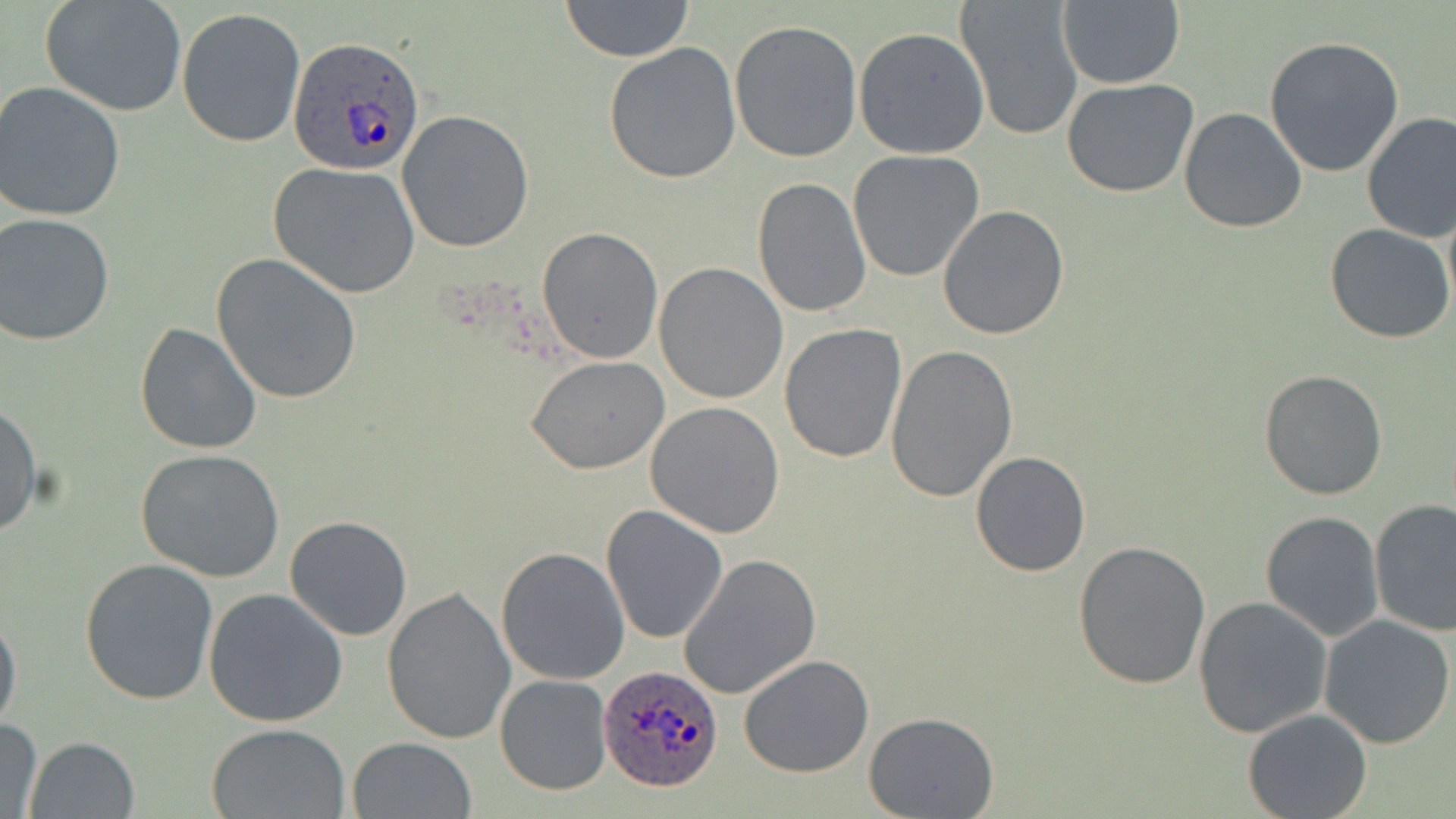

slide-level diagnosis = Plasmodium ovale
field of view = one of a larger specimen
uninfected red blood cell locations = approximate bounding boxes as (x1,y1)-(x2,y2) corner pairs in pixels: (40,0)-(189,118), (559,0)-(695,64), (954,0)-(1085,142), (1055,0)-(1185,89), (176,8)-(308,148), (728,19)-(862,163), (853,27)-(989,159), (1264,35)-(1405,178), (604,41)-(743,184), (1062,77)-(1199,198), (0,82)-(126,223), (1179,108)-(1307,231), (397,110)-(534,252), (1360,111)-(1456,243), (848,149)-(985,282), (268,162)-(420,298), (752,177)-(871,319), (938,204)-(1070,340), (1,214)-(115,346), (1325,224)-(1455,345), (536,226)-(665,364), (211,253)-(362,404), (654,261)-(788,403), (135,322)-(262,455), (780,323)-(908,464), (885,342)-(1019,503), (526,355)-(670,474), (1259,369)-(1387,501), (0,400)-(43,537), (646,401)-(785,538), (136,447)-(285,582), (969,450)-(1092,577), (1370,499)-(1456,636), (601,506)-(728,644), (1260,511)-(1384,642), (284,515)-(413,641), (1074,541)-(1210,689), (497,546)-(630,686), (679,553)-(822,701), (79,558)-(219,706), (382,585)-(516,746), (204,587)-(349,726), (1192,597)-(1334,738), (0,606)-(22,739), (1319,615)-(1455,748), (739,654)-(874,776), (494,674)-(612,795), (1242,709)-(1372,819), (865,712)-(998,819), (0,719)-(44,819), (206,723)-(352,818), (23,736)-(142,819), (346,736)-(476,819)
image size = 1456×819 pixels
stain = May-Grünwald-Giemsa
magnification = 1000x
Plasmodium ovale-infected red blood cell locations = approximate bounding boxes as (x1,y1)-(x2,y2) corner pairs in pixels: (288,34)-(426,176), (598,663)-(722,792)
preparation = thin blood smear
modality = light microscopy